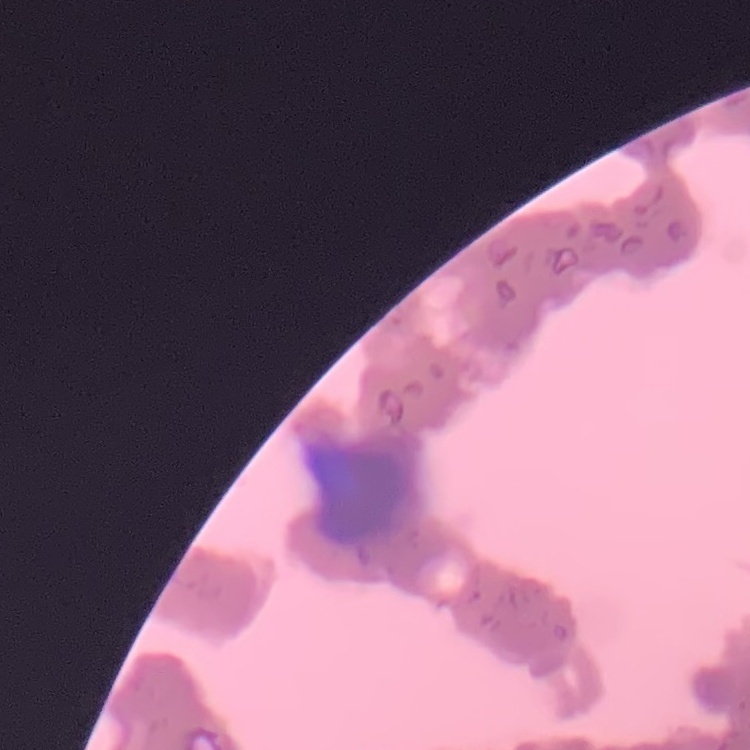

red_blood_cell_morphology: rouleaux formation
preparation: thin peripheral smear
stain: Field's or Giemsa
image_type: one tile cut from a larger photomicrograph